Classify this cell by malaria status.
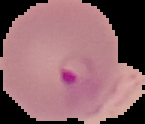

Parasitized.

The area outside the segmented cell region is set to black. From a thin blood smear. Image is 145×124 pixels.